Report the malaria status of this cell.
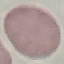
It is uninfected.

stain = Giemsa
image type = cell patch, automatically extracted from a larger field of view and resized to 64 × 64 pixels
capture = smartphone camera at the microscope eyepiece
preparation = thin blood film